Locate and identify every blood parasite.
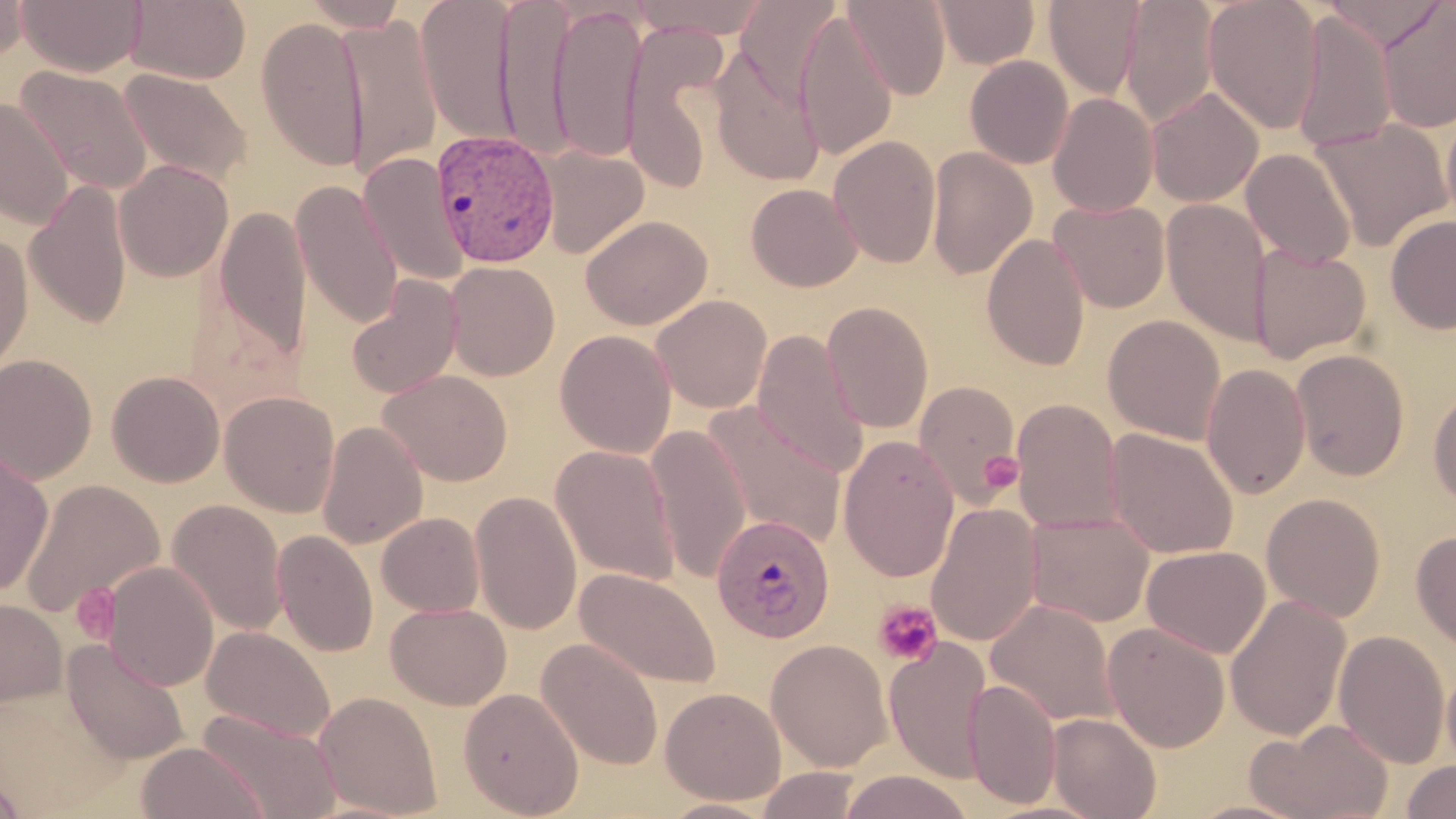
Approximate bounding boxes as (x1, y1, x2, y2) in pixels.
Plasmodium vivax-infected red blood cells: (433, 130, 560, 267), (712, 513, 835, 643).
No Plasmodium falciparum, Plasmodium ovale, Plasmodium malariae, Babesia divergens, or Trypanosoma brucei observed.

Summary:
  - Uninfected red blood cell locations: (0, 0, 30, 65), (17, 0, 146, 76), (125, 0, 251, 84), (416, 0, 520, 148), (495, 0, 574, 161), (630, 0, 773, 39), (843, 0, 950, 100), (932, 0, 1040, 69), (1121, 0, 1220, 128), (1203, 0, 1324, 134), (1322, 0, 1450, 51), (296, 1, 411, 30), (737, 1, 840, 108), (1043, 1, 1147, 101), (1376, 1, 1456, 134), (549, 3, 646, 163), (794, 9, 896, 160), (1290, 11, 1397, 154), (338, 13, 442, 182), (256, 16, 368, 175), (623, 26, 728, 196), (710, 47, 826, 187), (964, 55, 1074, 170), (16, 65, 154, 195), (118, 68, 252, 188), (1146, 87, 1264, 207), (1047, 93, 1158, 217), (0, 98, 74, 229), (1440, 99, 1456, 233), (1310, 119, 1452, 251), (828, 135, 941, 268), (535, 143, 649, 259), (925, 147, 1037, 280), (1241, 148, 1356, 268), (359, 152, 470, 287), (114, 159, 233, 281), (25, 178, 132, 330), (291, 179, 404, 331), (746, 182, 863, 291), (1049, 199, 1171, 313), (1161, 199, 1272, 346), (213, 203, 311, 366), (1385, 214, 1456, 334), (581, 215, 712, 330), (0, 231, 33, 381), (981, 232, 1091, 372), (1248, 244, 1371, 364), (444, 261, 560, 380), (346, 275, 463, 400), (651, 294, 772, 413), (822, 301, 934, 433), (1103, 314, 1226, 445), (555, 329, 676, 458), (752, 329, 869, 479), (1290, 349, 1410, 481), (0, 354, 97, 484), (1201, 362, 1311, 499), (106, 370, 225, 487), (379, 370, 512, 485), (914, 381, 1021, 504), (1428, 385, 1456, 509), (220, 391, 340, 518), (1011, 398, 1124, 534), (702, 403, 848, 546), (317, 421, 428, 549), (646, 424, 752, 582), (1105, 428, 1239, 560), (838, 435, 960, 583), (549, 444, 681, 586), (0, 449, 54, 596), (19, 478, 164, 620), (471, 489, 582, 635), (1261, 493, 1386, 622), (166, 499, 288, 636), (924, 501, 1043, 648), (377, 512, 485, 617), (1025, 512, 1154, 627), (272, 529, 378, 657), (1411, 529, 1456, 652), (1141, 545, 1270, 658), (101, 561, 219, 691), (575, 567, 723, 690), (1225, 595, 1351, 741), (0, 598, 67, 707), (985, 599, 1118, 728), (385, 602, 512, 710), (1102, 623, 1230, 752), (201, 625, 336, 743), (1333, 629, 1451, 769), (884, 636, 993, 783), (536, 638, 664, 771), (62, 639, 191, 764), (766, 639, 893, 771), (1442, 655, 1456, 775), (964, 677, 1062, 810), (458, 686, 584, 818), (660, 686, 786, 805), (313, 690, 444, 818), (198, 709, 343, 819), (1047, 712, 1161, 819), (1245, 718, 1395, 819), (135, 741, 270, 819), (1400, 759, 1456, 818), (754, 766, 865, 819), (838, 770, 974, 819), (0, 771, 29, 818), (656, 797, 779, 819), (1182, 798, 1314, 819)
  - Platelet locations: (980, 451, 1023, 495), (71, 584, 121, 644), (871, 599, 944, 667)
  - Slide-level diagnosis: Plasmodium vivax
  - Field of view: one of a larger specimen
  - Preparation: thin blood film
  - Modality: light microscopy
  - Image size: 1456×819 pixels
  - Stain: May-Grünwald-Giemsa
  - Magnification: 1000x